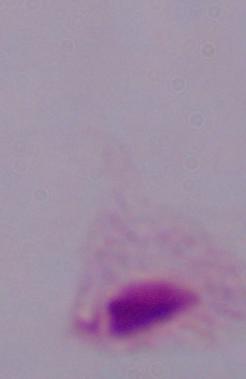

Summary:
  - Magnification: 1000x
  - Modality: photomicrograph
  - Identification: trichomonad